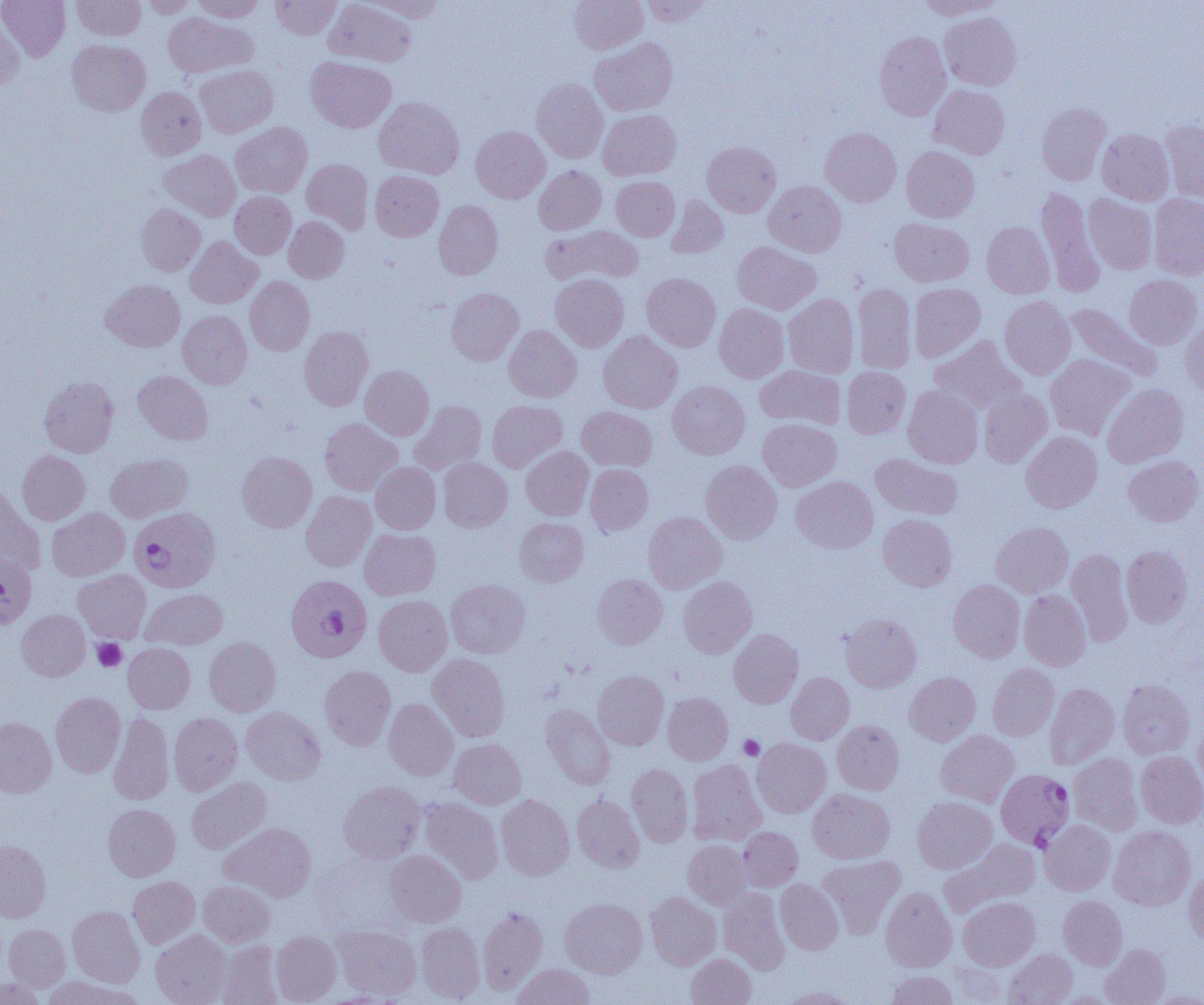
Summary:
  - Coordinate format: approximate bounding boxes as (x1, y1, x2, y2) in pixels
  - Platelet locations: (92, 639, 126, 672), (739, 735, 763, 760)
  - Plasmodium falciparum-infected red blood cell locations: (129, 507, 220, 592), (285, 574, 372, 662), (998, 770, 1077, 850)
  - Uninfected red blood cell locations: (0, 0, 70, 61), (71, 0, 146, 40), (142, 0, 197, 18), (192, 0, 264, 22), (271, 0, 341, 39), (324, 0, 417, 67), (363, 0, 446, 22), (569, 0, 648, 54), (641, 0, 712, 27), (916, 0, 1005, 19), (163, 12, 257, 77), (939, 12, 1022, 90), (0, 17, 23, 93), (874, 31, 951, 121), (589, 37, 678, 116), (67, 39, 150, 115), (306, 56, 396, 132), (196, 65, 278, 137), (531, 78, 608, 163), (928, 84, 1010, 159), (136, 87, 206, 160), (373, 97, 464, 178), (1037, 102, 1112, 185), (598, 109, 681, 180), (1160, 120, 1204, 202), (231, 122, 312, 198), (471, 126, 550, 203), (820, 127, 901, 206), (1097, 128, 1174, 205), (702, 141, 781, 217), (901, 146, 980, 222), (159, 150, 241, 221), (301, 158, 373, 233), (534, 165, 607, 235), (370, 170, 443, 241), (611, 176, 679, 241), (763, 180, 846, 257), (1037, 186, 1104, 296), (230, 191, 296, 258), (1148, 193, 1204, 279), (1083, 194, 1157, 274), (667, 196, 729, 258), (434, 200, 503, 280), (136, 203, 205, 276), (284, 216, 349, 282), (889, 218, 973, 287), (982, 221, 1054, 298), (541, 225, 643, 287), (185, 236, 262, 309), (732, 242, 821, 314), (641, 273, 721, 352), (550, 274, 629, 351), (1124, 274, 1203, 349), (245, 276, 315, 355), (101, 279, 185, 352), (852, 283, 916, 374), (909, 283, 986, 361), (446, 287, 523, 365), (783, 293, 859, 378), (999, 296, 1076, 379), (714, 303, 789, 383), (1064, 303, 1161, 382), (177, 310, 252, 388), (1180, 319, 1204, 398), (503, 325, 581, 402), (299, 326, 373, 411), (598, 330, 682, 413), (929, 335, 1027, 415), (1045, 354, 1136, 440), (360, 365, 434, 440), (755, 365, 845, 430), (842, 366, 910, 438), (133, 371, 213, 444), (40, 376, 118, 457), (667, 381, 750, 459), (1102, 384, 1189, 468), (902, 385, 983, 469), (979, 389, 1052, 467), (410, 400, 487, 474), (487, 400, 567, 472), (576, 406, 657, 471), (320, 418, 403, 496), (758, 418, 841, 491), (1021, 431, 1102, 513), (520, 447, 593, 520), (17, 451, 90, 525), (236, 451, 317, 532), (106, 453, 192, 522), (871, 453, 963, 520), (1123, 455, 1203, 526), (438, 457, 512, 532), (700, 460, 782, 544), (370, 462, 441, 534), (585, 464, 653, 535), (792, 476, 878, 553), (0, 485, 46, 573), (302, 491, 376, 571), (47, 508, 129, 581), (644, 511, 727, 593), (878, 514, 957, 591), (515, 517, 588, 586), (991, 521, 1073, 597), (359, 529, 440, 599), (1121, 546, 1193, 628), (1066, 549, 1133, 645), (0, 554, 36, 629), (73, 569, 151, 643), (592, 574, 668, 649), (678, 576, 757, 658), (446, 578, 530, 658), (948, 579, 1025, 662), (140, 589, 227, 649), (1019, 590, 1091, 670), (373, 595, 452, 676), (17, 609, 90, 681), (840, 614, 921, 692), (728, 629, 803, 707), (204, 637, 281, 716), (123, 643, 195, 713), (427, 654, 510, 741), (987, 664, 1059, 740), (319, 666, 396, 750), (593, 670, 669, 750), (786, 672, 854, 744), (905, 672, 980, 745), (1117, 678, 1194, 759), (1044, 683, 1119, 769), (51, 692, 125, 777), (663, 693, 733, 765), (384, 698, 458, 780), (539, 704, 615, 789), (241, 707, 325, 785), (109, 712, 174, 805), (169, 713, 243, 795), (0, 716, 56, 797), (832, 720, 904, 794), (1195, 721, 1204, 795), (936, 730, 1019, 807), (449, 738, 526, 809), (752, 738, 831, 818), (1136, 751, 1204, 828), (1069, 753, 1143, 835), (687, 759, 767, 845), (627, 764, 693, 846), (186, 777, 272, 854), (339, 781, 424, 864), (808, 789, 895, 864), (496, 794, 574, 880), (572, 795, 645, 872), (912, 796, 997, 873), (418, 797, 503, 884), (103, 803, 180, 881), (1040, 819, 1115, 895), (221, 822, 317, 902), (1108, 825, 1195, 910), (738, 827, 803, 891), (939, 838, 1041, 917), (0, 840, 51, 922), (683, 840, 751, 909), (385, 849, 466, 927), (817, 855, 905, 936), (1184, 869, 1204, 944), (128, 875, 200, 948), (775, 879, 844, 954), (198, 880, 275, 947), (880, 887, 956, 971), (717, 888, 790, 974), (645, 892, 721, 970), (1058, 895, 1127, 970), (959, 896, 1040, 970), (560, 898, 647, 978), (68, 906, 144, 987), (478, 906, 548, 994), (415, 922, 485, 1003), (4, 924, 70, 991), (332, 926, 421, 1000), (151, 930, 230, 1005), (271, 931, 341, 1004), (215, 940, 283, 1005), (1100, 944, 1171, 1005), (1003, 949, 1077, 1005), (686, 953, 756, 1005), (945, 962, 1006, 1004), (512, 963, 594, 1005), (887, 970, 957, 1005), (40, 975, 139, 1005), (0, 977, 47, 1004), (778, 986, 857, 1004), (1052, 990, 1121, 1004), (1145, 992, 1204, 1004)
  - Slide-level diagnosis: Plasmodium falciparum
  - Magnification: 1000x
  - Modality: optical microscopy
  - Field of view: one of a larger specimen
  - Image size: 1204×1005 pixels
  - Preparation: thin blood smear